State which parasite is depicted.
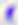
This is Toxoplasma gondii.

400x magnification. Micrograph.